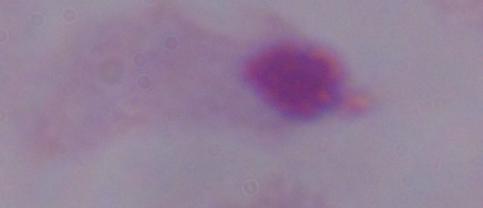

Summary:
  - Identification: trichomonad
  - Magnification: 1000x
  - Modality: micrograph